Locate every Plasmodium falciparum-infected red blood cell.
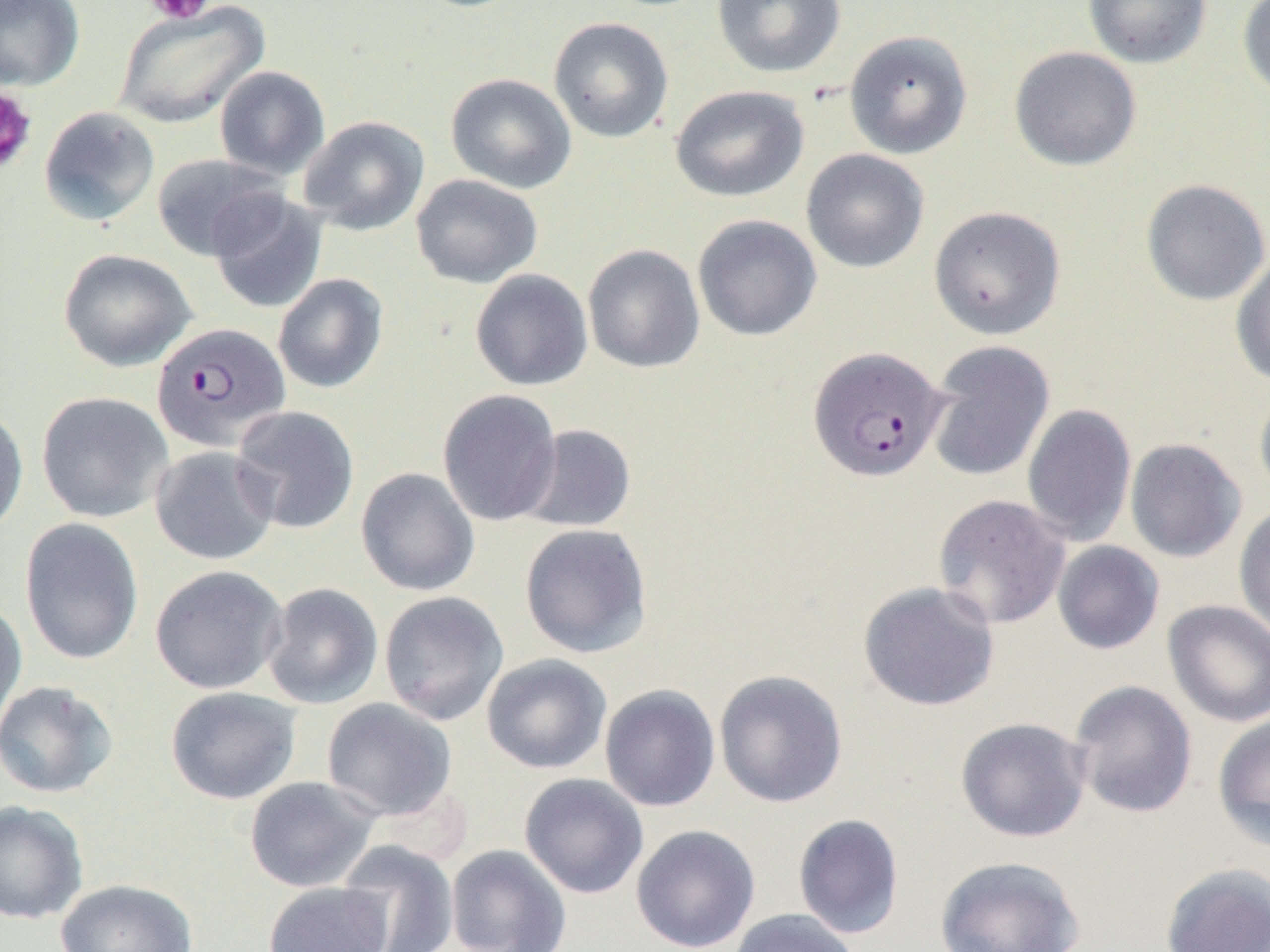

Approximate bounding boxes as named x1/y1/x2/y2 corners in pixels.
Plasmodium falciparum-infected red blood cells: (x1=150, y1=322, x2=290, y2=452), (x1=808, y1=346, x2=948, y2=483).

Platelet locations: (x1=143, y1=0, x2=217, y2=25), (x1=0, y1=85, x2=37, y2=175). Uninfected red blood cell locations: (x1=0, y1=0, x2=85, y2=91), (x1=712, y1=0, x2=847, y2=79), (x1=1082, y1=0, x2=1212, y2=69), (x1=1237, y1=0, x2=1270, y2=104), (x1=113, y1=1, x2=269, y2=130), (x1=548, y1=17, x2=673, y2=143), (x1=844, y1=29, x2=973, y2=159), (x1=1009, y1=46, x2=1141, y2=171), (x1=214, y1=65, x2=330, y2=180), (x1=445, y1=73, x2=577, y2=194), (x1=670, y1=85, x2=809, y2=202), (x1=38, y1=106, x2=160, y2=227), (x1=298, y1=116, x2=429, y2=236), (x1=801, y1=148, x2=930, y2=273), (x1=152, y1=153, x2=284, y2=261), (x1=411, y1=174, x2=543, y2=288), (x1=1140, y1=179, x2=1270, y2=306), (x1=207, y1=191, x2=328, y2=315), (x1=928, y1=205, x2=1066, y2=340), (x1=693, y1=215, x2=822, y2=341), (x1=582, y1=244, x2=705, y2=374), (x1=58, y1=248, x2=196, y2=372), (x1=1231, y1=252, x2=1270, y2=387), (x1=470, y1=269, x2=593, y2=391), (x1=273, y1=273, x2=388, y2=393), (x1=925, y1=341, x2=1055, y2=482), (x1=1254, y1=380, x2=1270, y2=502), (x1=437, y1=389, x2=562, y2=527), (x1=36, y1=391, x2=173, y2=523), (x1=1022, y1=403, x2=1136, y2=547), (x1=0, y1=405, x2=28, y2=539), (x1=230, y1=405, x2=360, y2=534), (x1=518, y1=423, x2=636, y2=533), (x1=1125, y1=438, x2=1247, y2=562), (x1=149, y1=445, x2=279, y2=566), (x1=356, y1=467, x2=480, y2=596), (x1=932, y1=494, x2=1071, y2=630), (x1=1233, y1=503, x2=1270, y2=643), (x1=19, y1=517, x2=144, y2=665), (x1=519, y1=523, x2=653, y2=659), (x1=1052, y1=541, x2=1165, y2=655), (x1=149, y1=565, x2=288, y2=694), (x1=857, y1=580, x2=1000, y2=712), (x1=261, y1=582, x2=384, y2=710), (x1=378, y1=590, x2=509, y2=726), (x1=0, y1=599, x2=27, y2=732), (x1=1163, y1=600, x2=1270, y2=728), (x1=481, y1=654, x2=612, y2=774), (x1=714, y1=669, x2=848, y2=808), (x1=1069, y1=679, x2=1198, y2=819), (x1=0, y1=681, x2=119, y2=799), (x1=599, y1=684, x2=720, y2=812), (x1=164, y1=687, x2=302, y2=805), (x1=321, y1=698, x2=458, y2=821), (x1=1212, y1=712, x2=1270, y2=853), (x1=955, y1=717, x2=1091, y2=842), (x1=519, y1=773, x2=649, y2=899), (x1=244, y1=776, x2=379, y2=893), (x1=0, y1=800, x2=89, y2=924), (x1=792, y1=813, x2=905, y2=939), (x1=630, y1=823, x2=761, y2=952), (x1=337, y1=840, x2=459, y2=952), (x1=446, y1=844, x2=572, y2=952), (x1=934, y1=854, x2=1085, y2=951), (x1=1160, y1=862, x2=1270, y2=952), (x1=55, y1=878, x2=197, y2=952), (x1=263, y1=882, x2=393, y2=952), (x1=728, y1=908, x2=862, y2=952). Slide-level diagnosis: Plasmodium falciparum. Optical microscopy. Single field of view. 1000x magnification. Image is 1270×952 pixels. Thin blood film.